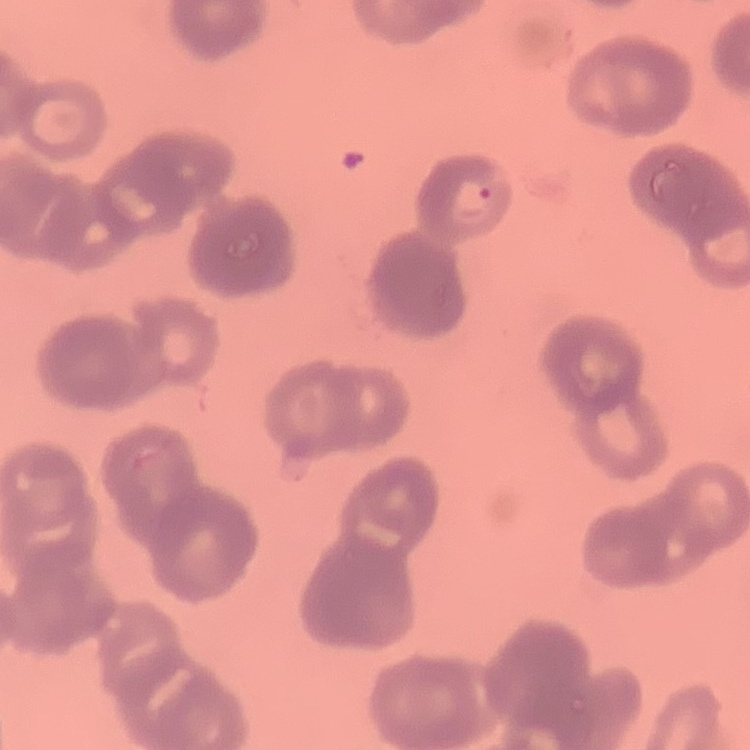
red_blood_cell_morphology: rouleaux formation
preparation: thin blood smear
stain: Field's or Giemsa
image_type: square crop of a larger photomicrograph